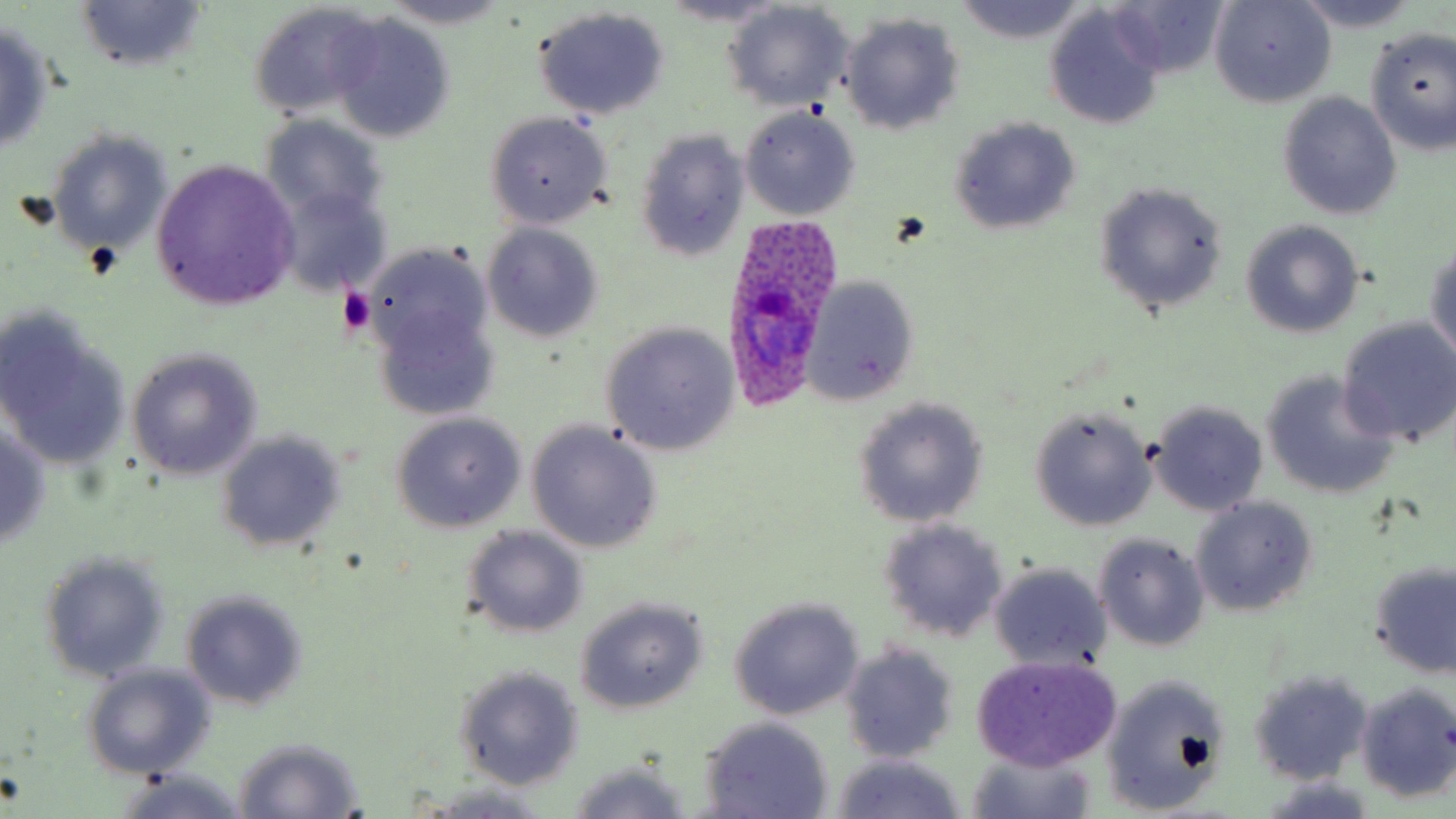
Approximate bounding boxes as [x1, y1, x2, y2] in pixels. Platelet locations: [337, 286, 375, 335]. Uninfected red blood cell locations: [1101, 0, 1229, 80], [1209, 0, 1335, 108], [1289, 0, 1425, 32], [377, 1, 519, 31], [658, 1, 794, 30], [953, 1, 1083, 42], [74, 2, 207, 72], [721, 3, 854, 111], [247, 4, 384, 123], [533, 6, 671, 120], [1043, 9, 1166, 130], [840, 12, 965, 136], [327, 14, 457, 143], [0, 20, 56, 154], [1364, 28, 1456, 153], [1277, 92, 1402, 222], [740, 107, 860, 220], [484, 111, 613, 230], [261, 116, 390, 227], [947, 117, 1081, 237], [633, 128, 748, 262], [48, 131, 173, 258], [151, 160, 301, 309], [1093, 182, 1228, 317], [272, 184, 391, 297], [1242, 219, 1365, 338], [482, 223, 604, 344], [1426, 241, 1456, 365], [365, 259, 501, 418], [801, 275, 920, 405], [0, 315, 130, 474], [1337, 319, 1456, 447], [600, 323, 739, 456], [127, 348, 262, 480], [1260, 370, 1399, 500], [852, 398, 989, 527], [1147, 400, 1268, 516], [1030, 407, 1156, 531], [391, 412, 526, 532], [526, 420, 663, 554], [0, 421, 53, 551], [216, 431, 345, 552], [1190, 496, 1319, 616], [877, 518, 1009, 644], [461, 526, 588, 638], [1094, 533, 1211, 651], [38, 549, 170, 684], [1367, 560, 1456, 678], [988, 562, 1113, 675], [180, 588, 309, 711], [729, 597, 863, 721], [575, 598, 708, 714], [840, 641, 961, 762], [971, 656, 1123, 770], [80, 663, 215, 779], [453, 665, 583, 790], [1248, 667, 1372, 786], [1101, 672, 1231, 816], [1354, 680, 1456, 803], [697, 716, 834, 818], [232, 736, 364, 818], [967, 747, 1097, 819], [828, 753, 966, 819], [566, 763, 693, 819], [115, 770, 251, 819], [1256, 777, 1381, 818], [416, 782, 562, 816]. Plasmodium ovale-infected red blood cell locations: [728, 218, 839, 410]. Slide-level diagnosis: Plasmodium ovale. Single field of view. Captured at 1000x magnification. Optical microscopy. Thin blood smear. May-Grünwald-Giemsa-stained preparation. Image is 1456×819 pixels.